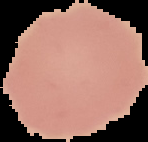

Summary:
  - Preparation: thin blood smear
  - Image type: segmented cell region with the area outside set to black
  - Malaria status: uninfected
  - Image size: 148×142 pixels